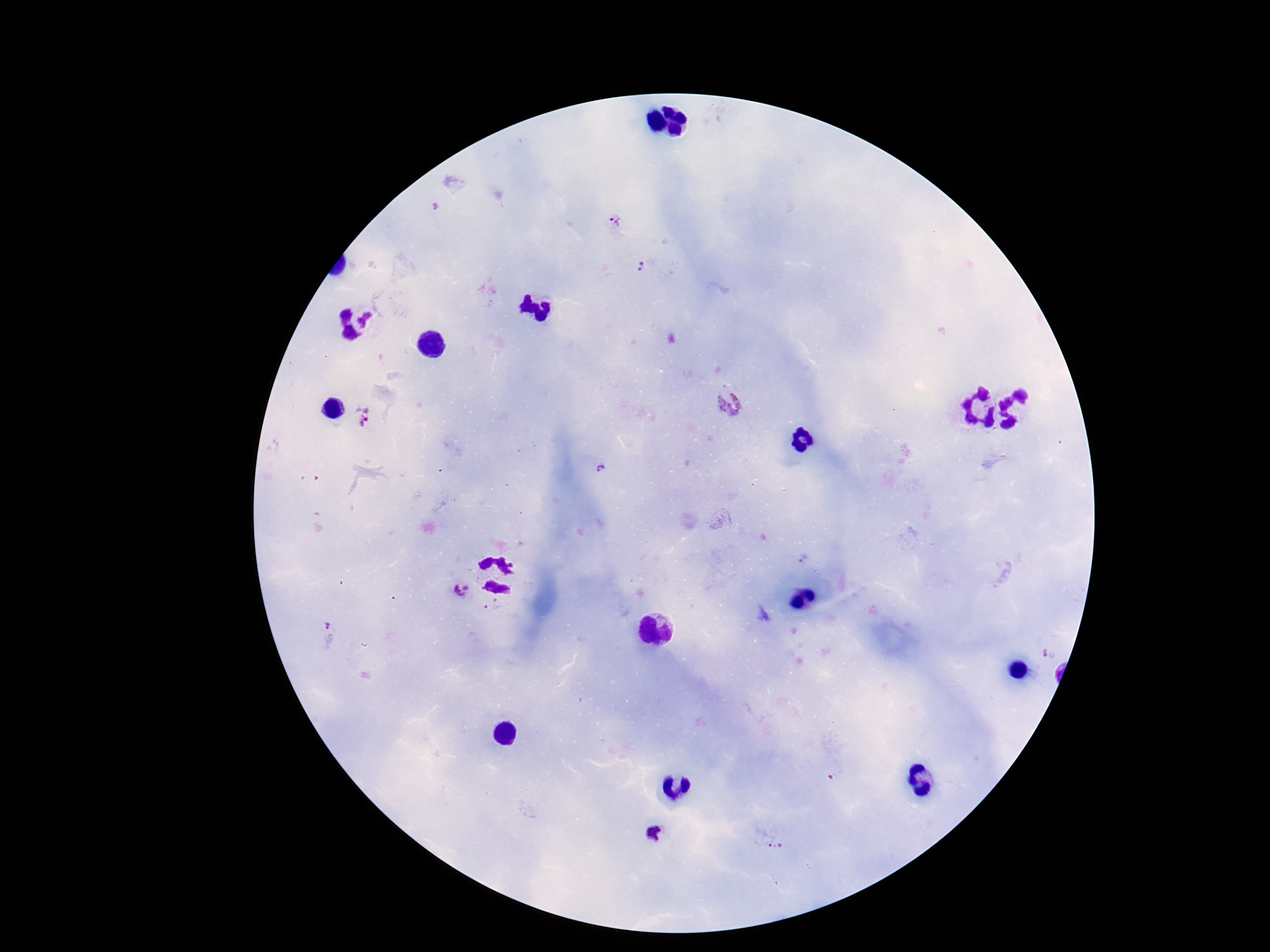

Approximate centers as {x, y} in pixels. Plasmodium parasite locations: {436, 207}, {618, 224}, {644, 269}, {729, 402}, {363, 420}, {604, 469}, {803, 558}, {455, 590}, {494, 609}, {324, 624}, {1050, 655}, {657, 834}, {769, 840}. 100x magnification. Photographed through the microscope eyepiece with a smartphone camera. Patient malaria status: positive. Image is 1270×952 pixels. Giemsa stain. One field from this slide. Thick blood film.